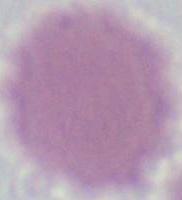
Summary:
  - Identification: red blood cell
  - Modality: photomicrograph
  - Magnification: 1000x